Identify the cell.
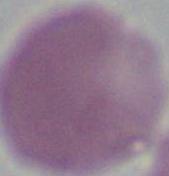

An erythrocyte.

magnification = 1000x
modality = photomicrograph